Outline each blood parasite and name the species.
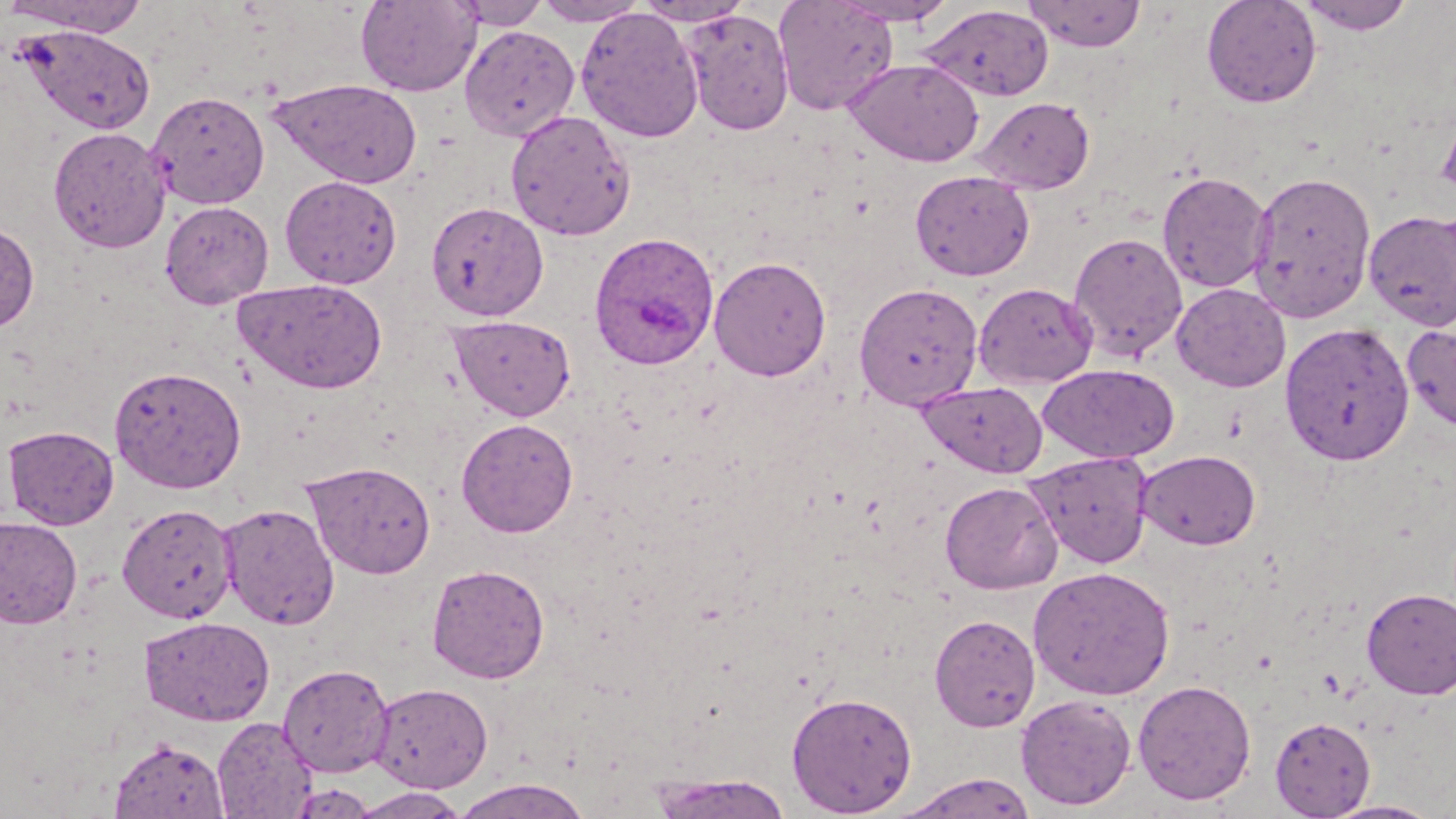
Approximate bounding boxes as named x1/y1/x2/y2 corners in pixels.
Plasmodium ovale-infected red blood cells: (x1=587, y1=235, x2=718, y2=373).
No Plasmodium falciparum, Plasmodium malariae, Plasmodium vivax, Babesia divergens, or Trypanosoma brucei observed.

slide_level_diagnosis: Plasmodium ovale
modality: optical microscopy
uninfected_red_blood_cell_locations: 'approximate bounding boxes as named x1/y1/x2/y2 corners in pixels: (x1=2, y1=0, x2=151, y2=37), (x1=356, y1=0, x2=481, y2=97), (x1=452, y1=0, x2=550, y2=29), (x1=634, y1=0, x2=752, y2=26), (x1=773, y1=0, x2=899, y2=116), (x1=830, y1=0, x2=959, y2=26), (x1=1022, y1=0, x2=1147, y2=52), (x1=1201, y1=0, x2=1323, y2=109), (x1=1295, y1=0, x2=1417, y2=35), (x1=533, y1=1, x2=648, y2=26), (x1=921, y1=5, x2=1054, y2=102), (x1=575, y1=7, x2=705, y2=144), (x1=681, y1=9, x2=794, y2=135), (x1=15, y1=24, x2=155, y2=136), (x1=459, y1=25, x2=580, y2=141), (x1=843, y1=59, x2=984, y2=167), (x1=268, y1=78, x2=422, y2=189), (x1=148, y1=90, x2=270, y2=209), (x1=974, y1=96, x2=1096, y2=195), (x1=1435, y1=109, x2=1456, y2=205), (x1=505, y1=110, x2=636, y2=241), (x1=48, y1=127, x2=170, y2=252), (x1=910, y1=170, x2=1035, y2=281), (x1=1247, y1=170, x2=1377, y2=324), (x1=1156, y1=171, x2=1272, y2=294), (x1=280, y1=175, x2=402, y2=289), (x1=160, y1=201, x2=274, y2=307), (x1=426, y1=201, x2=548, y2=321), (x1=1363, y1=210, x2=1456, y2=331), (x1=0, y1=222, x2=39, y2=333), (x1=1068, y1=232, x2=1188, y2=363), (x1=709, y1=255, x2=832, y2=381), (x1=234, y1=278, x2=387, y2=394), (x1=854, y1=282, x2=984, y2=410), (x1=973, y1=282, x2=1098, y2=389), (x1=1171, y1=283, x2=1291, y2=392), (x1=447, y1=315, x2=576, y2=421), (x1=1279, y1=321, x2=1415, y2=466), (x1=1402, y1=321, x2=1456, y2=434), (x1=1039, y1=364, x2=1179, y2=463), (x1=109, y1=365, x2=247, y2=494), (x1=916, y1=381, x2=1048, y2=477), (x1=456, y1=418, x2=578, y2=537), (x1=2, y1=425, x2=119, y2=529), (x1=1137, y1=449, x2=1261, y2=550), (x1=1024, y1=450, x2=1154, y2=569), (x1=303, y1=460, x2=436, y2=579), (x1=940, y1=480, x2=1064, y2=595), (x1=218, y1=502, x2=340, y2=630), (x1=117, y1=503, x2=237, y2=623), (x1=0, y1=517, x2=82, y2=629), (x1=427, y1=563, x2=550, y2=683), (x1=1028, y1=566, x2=1176, y2=700), (x1=1361, y1=587, x2=1456, y2=699), (x1=930, y1=613, x2=1041, y2=732), (x1=139, y1=616, x2=275, y2=726), (x1=278, y1=663, x2=393, y2=777), (x1=1133, y1=679, x2=1257, y2=805), (x1=368, y1=682, x2=494, y2=793), (x1=787, y1=691, x2=918, y2=816), (x1=1016, y1=694, x2=1137, y2=810), (x1=212, y1=716, x2=317, y2=818), (x1=1269, y1=716, x2=1377, y2=818), (x1=110, y1=738, x2=229, y2=818), (x1=894, y1=772, x2=1039, y2=819), (x1=647, y1=773, x2=795, y2=818), (x1=451, y1=777, x2=592, y2=819), (x1=347, y1=787, x2=472, y2=818), (x1=1321, y1=799, x2=1445, y2=819)'
image_size: 1456×819 pixels
stain: May-Grünwald-Giemsa
preparation: thin blood smear
field_of_view: single
magnification: 1000x